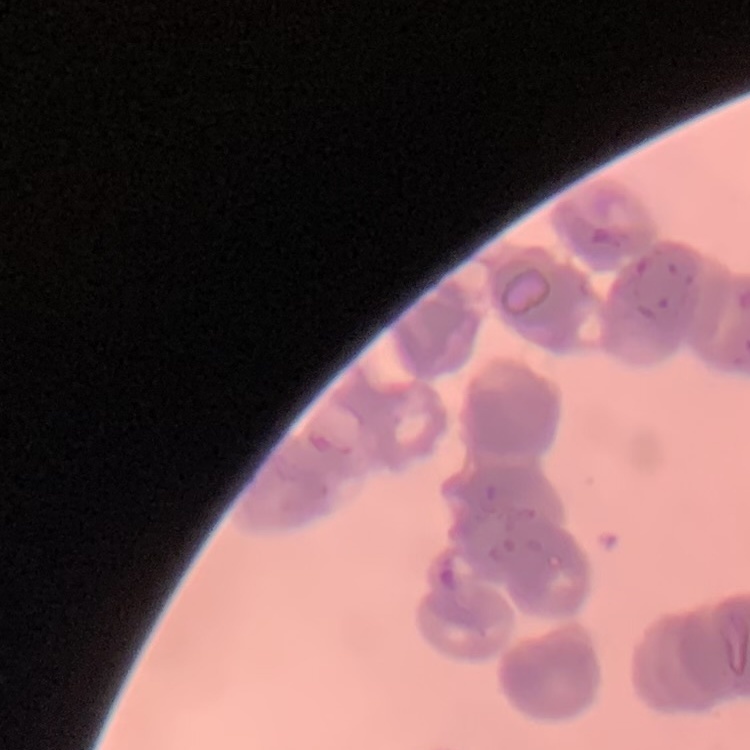

erythrocyte morphology = rouleaux formation
image type = square crop of a larger photomicrograph
stain = Field's or Giemsa
preparation = thin blood film